Give the position of every malaria parasite, noting whether each is a trophozoite, schizont, or gametocyte.
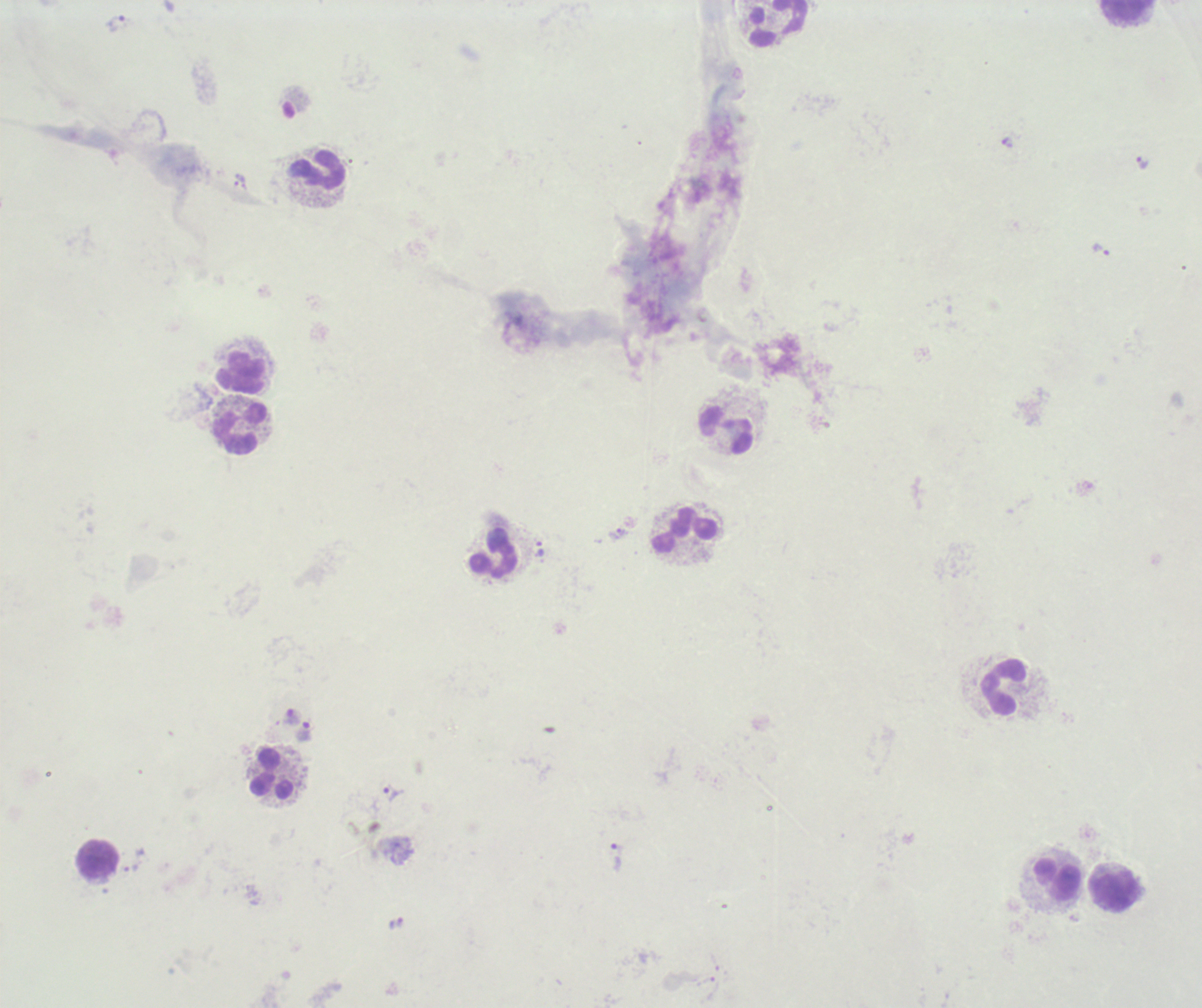
Approximate centers as {x, y} in pixels.
Trophozoites: {119, 23}, {1007, 143}, {1141, 163}, {1101, 250}, {617, 533}, {289, 716}, {304, 732}, {393, 793}, {614, 857}, {132, 868}.
No schizont or gametocyte forms observed.

leukocyte_locations: 'approximate centers as {x, y} in pixels: {1126, 11}, {777, 24}, {317, 170}, {242, 373}, {238, 428}, {726, 432}, {684, 530}, {494, 553}, {1004, 687}, {272, 774}, {98, 860}, {1056, 880}, {1113, 892}'
stain: Romanowsky
field_of_view: single
context: previously used in a real diagnosis
preparation: thick blood film
background_quality: poor
image_size: 1202×1008 pixels
magnification: 100x